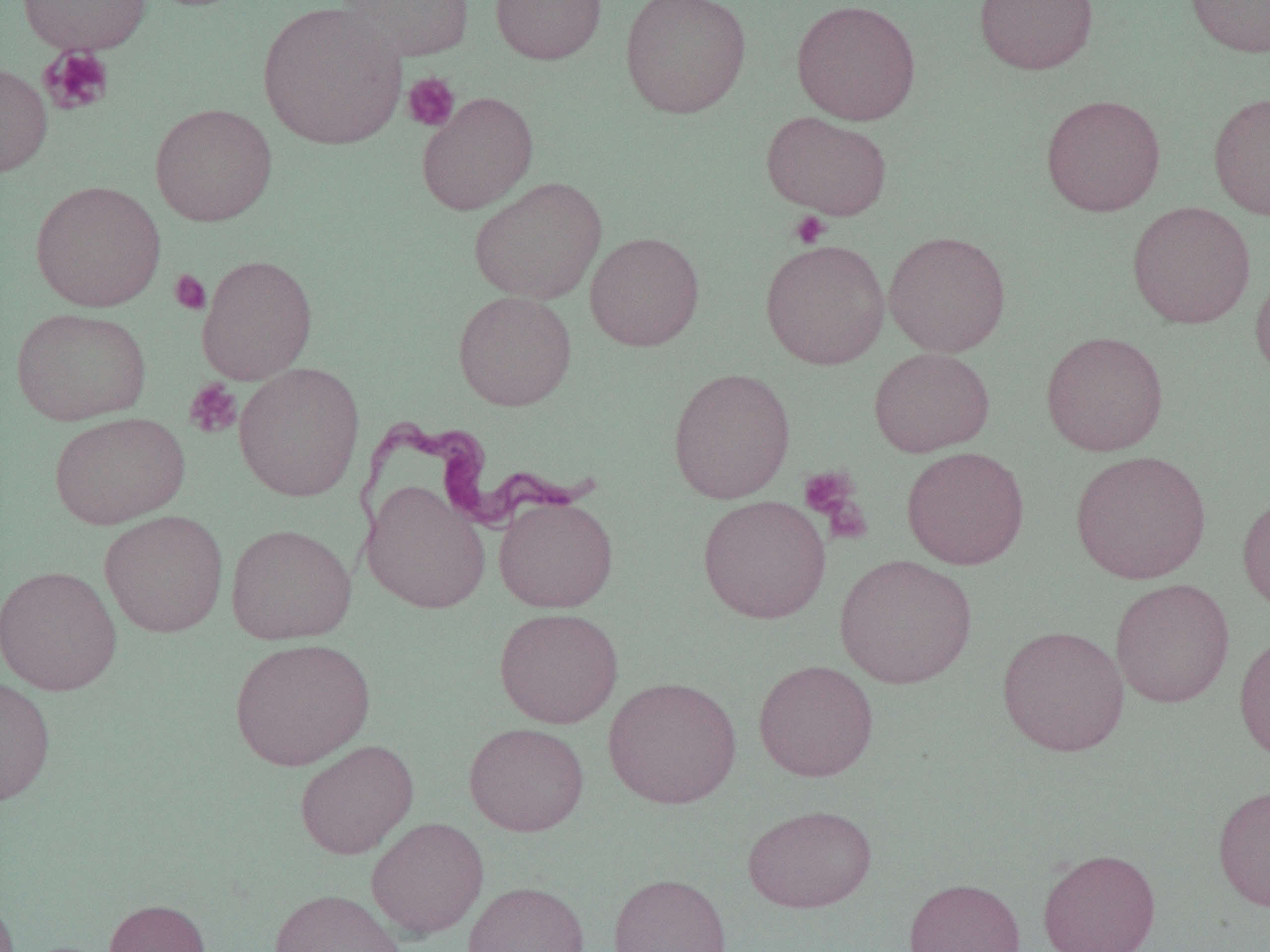

{
  "slide_level_diagnosis": "Trypanosoma brucei",
  "uninfected_red_blood_cell_locations_subset": "approximate bounding boxes as [x1, y1, x2, y2] in pixels: [17, 0, 152, 55], [336, 0, 475, 62], [490, 0, 607, 65], [620, 0, 751, 119], [791, 0, 921, 126], [974, 0, 1098, 75], [1184, 0, 1270, 58], [257, 2, 407, 150], [0, 63, 53, 178], [416, 91, 538, 215], [1208, 91, 1270, 221], [1041, 93, 1166, 216], [150, 103, 278, 226], [762, 111, 892, 219], [467, 176, 607, 305], [31, 180, 166, 312], [1127, 201, 1256, 329], [584, 231, 705, 351], [884, 231, 1011, 357], [760, 239, 890, 369], [1250, 265, 1270, 384], [453, 290, 576, 411], [11, 307, 151, 426], [1041, 330, 1169, 456], [869, 347, 994, 457], [233, 362, 366, 502], [667, 367, 796, 504], [49, 411, 190, 529], [901, 446, 1030, 570], [1070, 450, 1211, 584], [361, 480, 490, 614], [1237, 490, 1270, 615], [493, 494, 618, 612], [698, 495, 831, 624], [99, 509, 228, 638], [225, 523, 357, 645], [834, 554, 977, 689], [0, 563, 123, 696], [1111, 578, 1235, 707], [494, 607, 624, 729], [996, 624, 1130, 757], [1234, 630, 1270, 765], [229, 637, 375, 771], [753, 659, 879, 782], [0, 676, 56, 806], [603, 676, 742, 809], [464, 722, 589, 836], [294, 739, 419, 859], [1213, 784, 1270, 911], [742, 804, 877, 913], [366, 817, 489, 939], [1037, 847, 1161, 952], [608, 872, 732, 952], [903, 877, 1026, 952], [462, 881, 589, 952], [0, 888, 19, 951], [269, 888, 408, 952], [103, 898, 211, 952]",
  "modality": "light microscopy",
  "field_of_view": "one of a larger specimen",
  "image_size": "1270×952 pixels",
  "magnification": "1000x",
  "platelet_locations_subset": "approximate bounding boxes as [x1, y1, x2, y2] in pixels: [39, 46, 115, 116], [402, 72, 461, 132], [788, 211, 832, 249], [169, 269, 211, 315], [184, 379, 242, 439], [799, 465, 863, 523]",
  "preparation": "thin blood film",
  "trypanosoma_brucei_locations": "approximate bounding boxes as [x1, y1, x2, y2] in pixels: [352, 420, 602, 548]"
}